Report the malaria status of this cell.
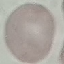
Uninfected.

stain = Giemsa
preparation = thin smear
image type = cell patch, automatically extracted from a larger field of view and resized to 64 × 64 pixels
capture = smartphone camera at the microscope eyepiece